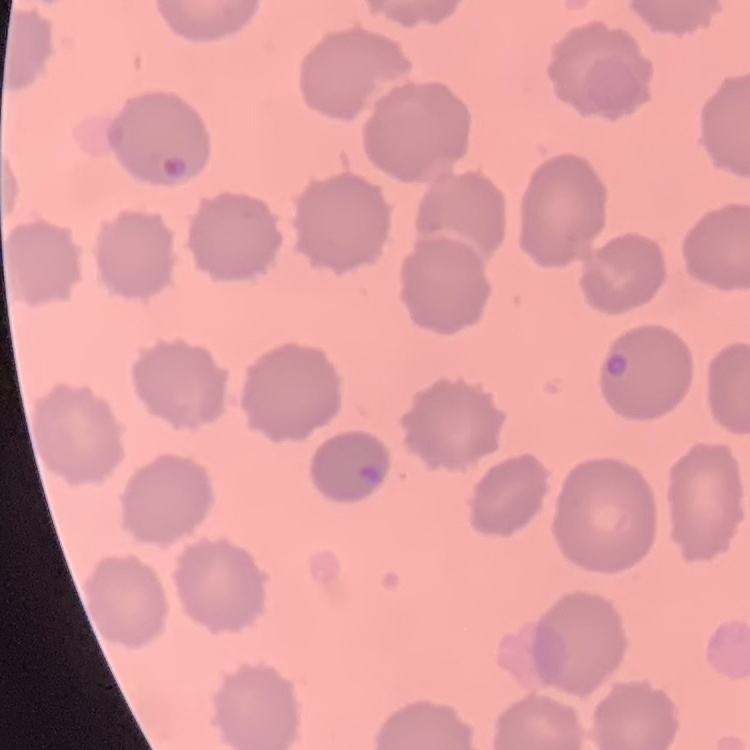
The red blood cells exhibit no rouleaux formation. Stained with either Field's or Giemsa. One tile cut from a larger photomicrograph. Thin blood smear.